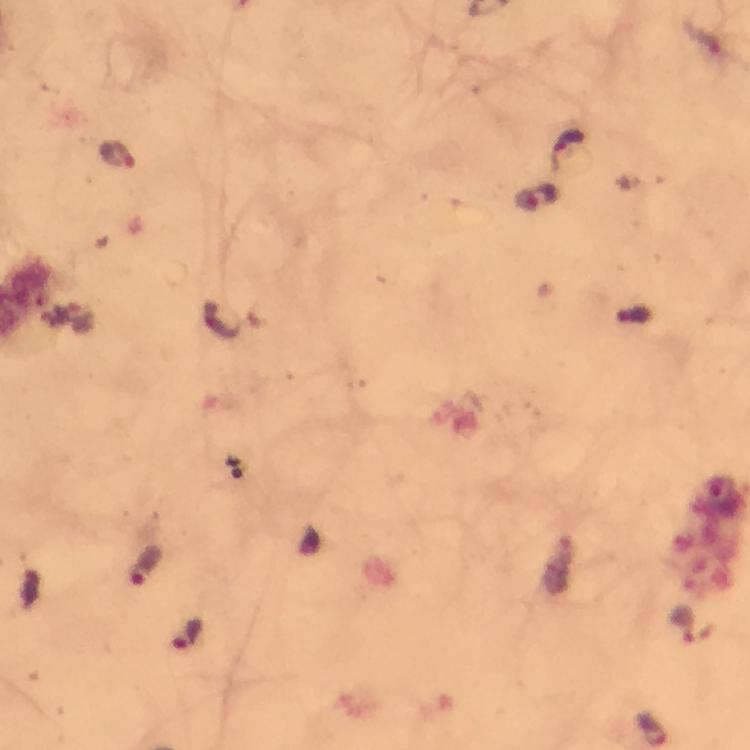

magnification = 100x
malaria parasite locations = approximate centers as (x, y) in pixels: (568, 148), (116, 155), (542, 198), (146, 566), (683, 624), (188, 634)
preparation = thick blood film
context = from a diagnostic examination for malaria
cropped from = one field of view
image size = 750×750 pixels
stain = Giemsa
immersion oil = applied
capture = smartphone camera through the microscope